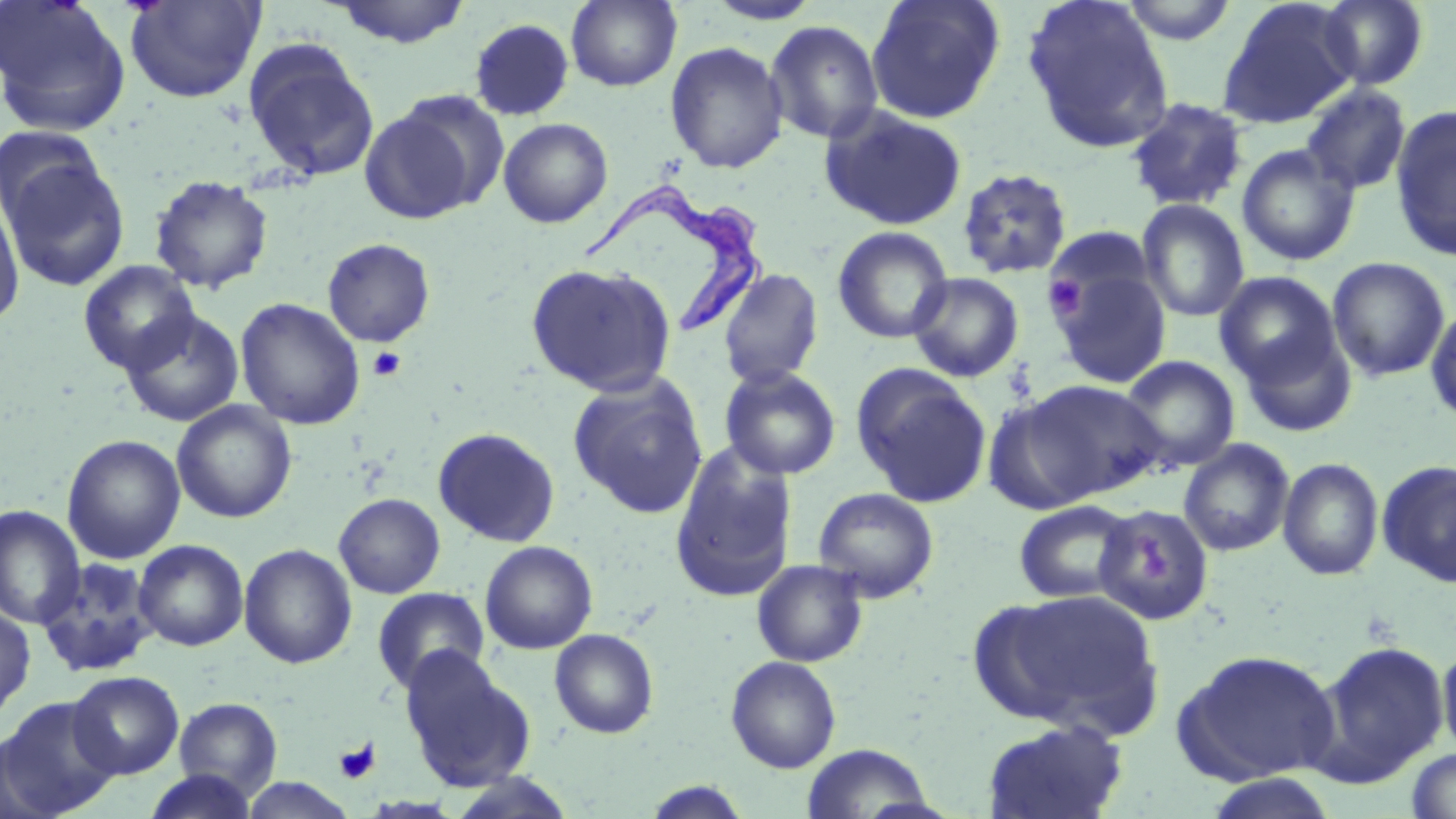
Approximate bounding boxes as (x1, y1, x2, y2) in pixels. Trypanosoma brucei locations: (578, 185, 776, 340). Platelet locations: (1044, 275, 1087, 323), (367, 346, 407, 382), (333, 738, 381, 785). Uninfected red blood cell locations: (0, 0, 131, 136), (125, 0, 265, 104), (330, 0, 471, 48), (566, 0, 682, 91), (705, 0, 823, 25), (866, 0, 1005, 124), (1022, 0, 1175, 155), (1120, 0, 1239, 45), (1217, 0, 1357, 129), (1318, 0, 1429, 90), (469, 18, 574, 121), (765, 20, 884, 144), (243, 38, 379, 183), (664, 41, 789, 174), (1300, 83, 1412, 196), (360, 95, 500, 223), (1125, 97, 1249, 211), (1389, 104, 1456, 262), (819, 105, 969, 231), (498, 117, 613, 228), (0, 125, 110, 235), (1236, 144, 1360, 266), (2, 156, 130, 291), (956, 167, 1073, 280), (150, 175, 274, 293), (0, 194, 25, 329), (1137, 199, 1250, 322), (832, 226, 954, 344), (323, 238, 435, 346), (1326, 256, 1451, 382), (78, 260, 199, 375), (525, 261, 676, 398), (1050, 264, 1172, 389), (718, 268, 824, 389), (1213, 270, 1344, 392), (907, 272, 1024, 383), (235, 298, 365, 430), (1425, 301, 1456, 427), (120, 309, 244, 427), (1235, 322, 1358, 438), (1119, 355, 1240, 473), (850, 364, 992, 509), (720, 365, 841, 481), (568, 374, 708, 519), (1020, 379, 1167, 502), (982, 394, 1100, 515), (172, 400, 297, 523), (432, 427, 561, 548), (62, 434, 185, 564), (1178, 438, 1294, 557), (669, 441, 799, 603), (1278, 457, 1384, 581), (1376, 459, 1456, 587), (812, 486, 939, 603), (334, 493, 445, 598), (1013, 500, 1137, 603), (1093, 504, 1215, 625), (0, 505, 85, 629), (134, 539, 248, 651), (480, 541, 598, 654), (239, 543, 357, 669), (36, 557, 160, 678), (751, 559, 869, 668), (371, 587, 490, 694), (987, 588, 1165, 735), (0, 604, 36, 721), (549, 628, 659, 739), (1309, 640, 1449, 786), (1437, 643, 1456, 764), (399, 647, 536, 791), (1175, 649, 1342, 785), (725, 656, 842, 773), (67, 670, 184, 779), (0, 696, 121, 817), (173, 697, 283, 797), (981, 718, 1130, 819), (0, 732, 63, 819), (800, 743, 934, 818), (1405, 747, 1456, 817), (142, 770, 260, 819), (1201, 773, 1341, 819), (237, 776, 359, 818), (640, 780, 753, 818). Slide-level diagnosis: Trypanosoma brucei. 1000x magnification. Thin blood smear. Image is 1456×819 pixels. One field of a larger specimen. Light microscopy. May-Grünwald-Giemsa stain.